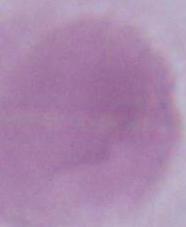 1000x magnification. Micrograph. A red blood cell is seen.